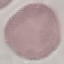
malaria status = uninfected
preparation = thin smear
stain = Giemsa
capture = smartphone camera at the microscope eyepiece
image type = cell patch, automatically extracted from a larger field of view and resized to 64 × 64 pixels